Locate every Plasmodium parasite.
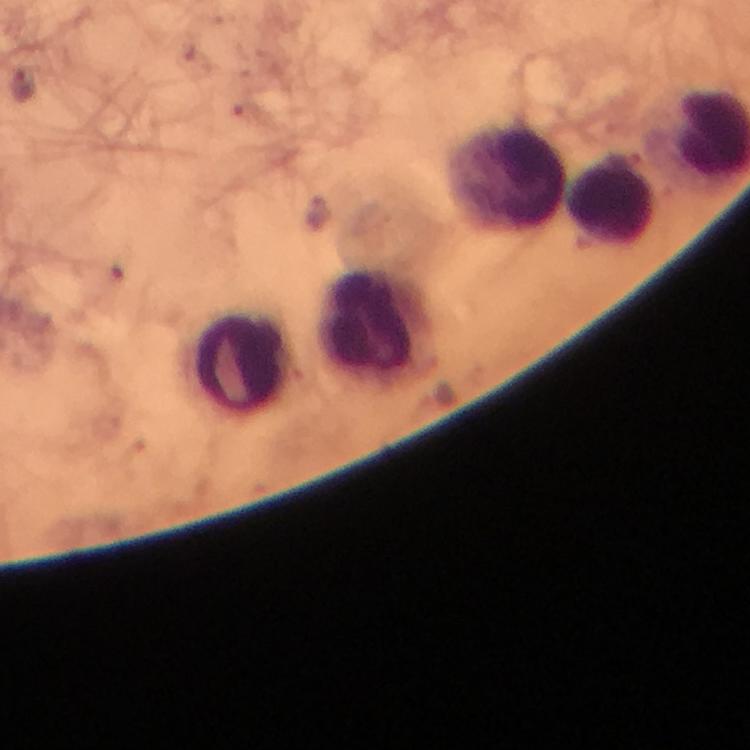

Approximate centers as {x, y} in pixels.
Plasmodium parasites: {24, 85}.

immersion oil = used
image size = 750×750 pixels
stain = Giemsa
capture = smartphone camera through the microscope
context = from a malaria diagnostic workup
magnification = 100x
preparation = thick smear
leukocyte locations = approximate centers as {x, y} in pixels: {504, 176}, {611, 200}, {374, 326}, {241, 362}
cropped from = one field of view